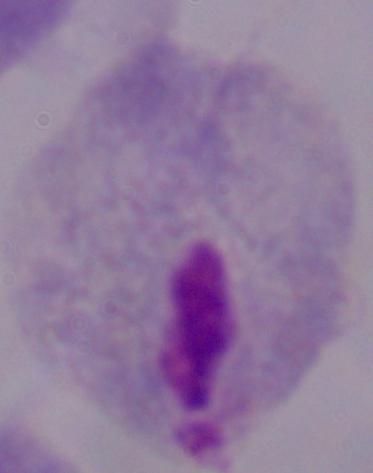

Summary:
  - Modality: micrograph
  - Identification: trichomonad
  - Magnification: 1000x